Point out Plasmodium parasites and leukocytes.
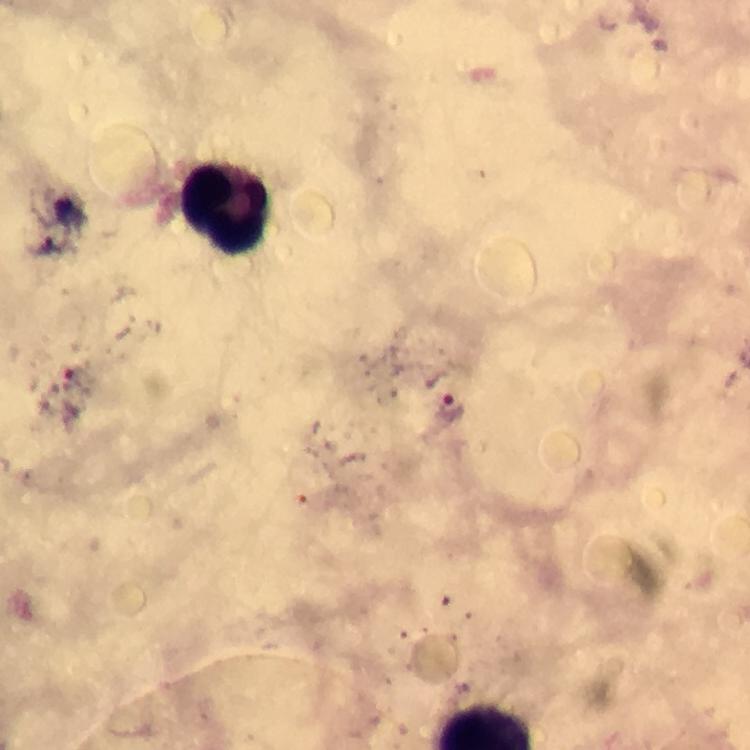

Approximate object centers, in pixels from the top-left corner.
Plasmodium parasites: (x=71, y=379), (x=454, y=406).
Leukocytes: (x=225, y=210).

From a malaria diagnostic workup. At 100x magnification. Image is 750×750 pixels. Giemsa-stained preparation. Immersion oil applied. A crop from one field of view. Photographed with a smartphone mounted on the microscope. Thick blood smear.